Name the parasite shown.
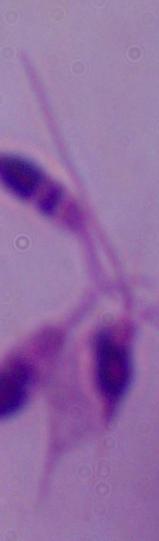

Leishmania.

Summary:
  - Modality: photomicrograph
  - Magnification: 1000x